State the blood parasite species.
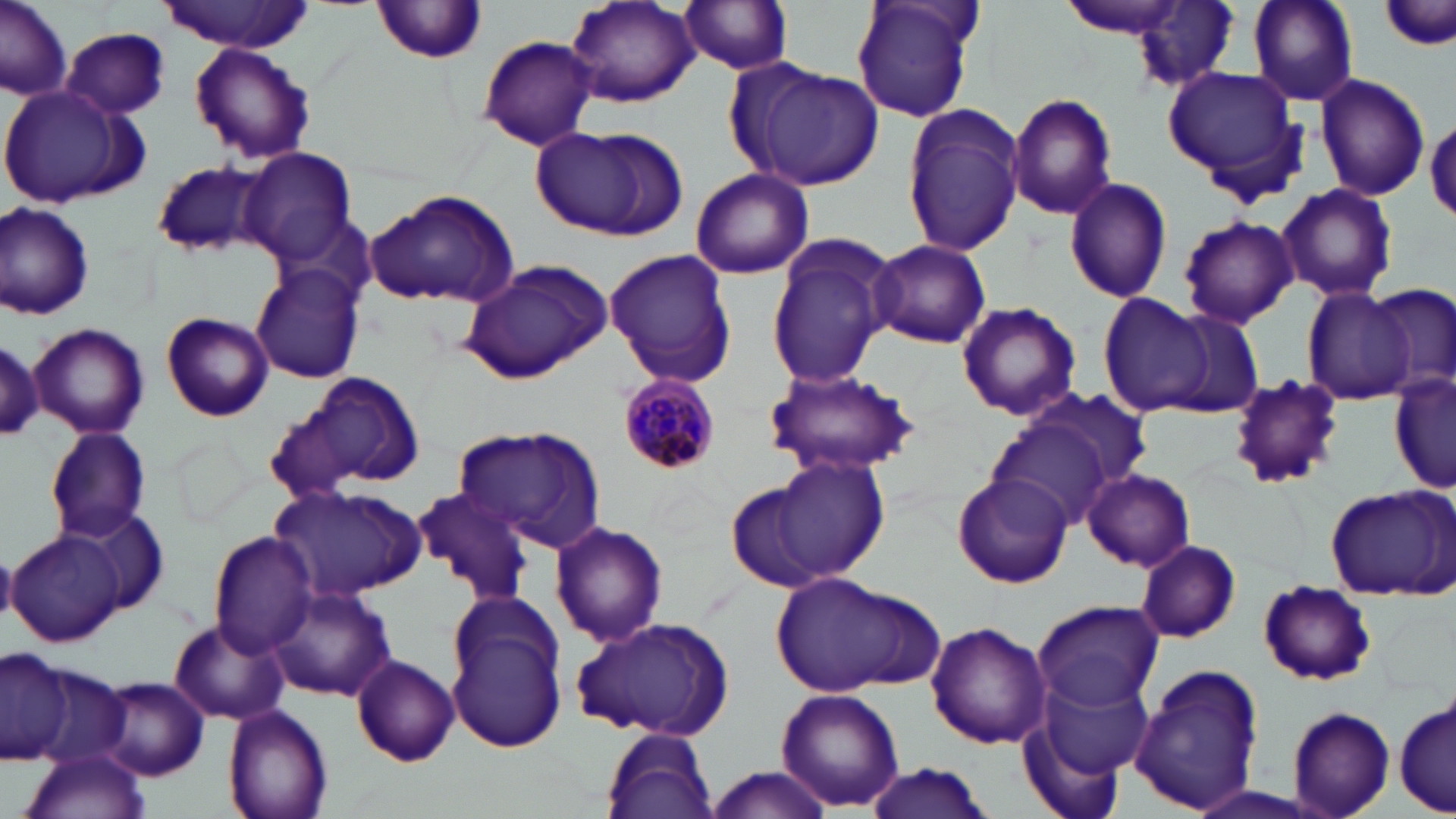

Plasmodium malariae.

Summary:
  - Coordinate format: approximate bounding boxes as (x1,y1)-(x2,y2) corner pairs in pixels
  - Plasmodium malariae-infected red blood cell locations: (619,381)-(718,472)
  - Uninfected red blood cell locations: (0,0)-(72,99), (562,0)-(700,107), (849,0)-(983,125), (1248,0)-(1358,106), (678,1)-(797,74), (1378,1)-(1456,53), (159,2)-(316,52), (371,2)-(489,65), (1127,2)-(1243,91), (60,26)-(172,119), (477,35)-(599,152), (190,44)-(316,164), (744,64)-(886,189), (1162,68)-(1304,177), (1314,71)-(1430,201), (0,85)-(150,208), (1007,91)-(1118,218), (901,104)-(1026,258), (1426,114)-(1456,221), (531,125)-(681,240), (237,146)-(358,264), (150,159)-(271,259), (690,169)-(814,279), (1063,175)-(1173,304), (1277,182)-(1399,302), (364,189)-(521,309), (0,200)-(96,320), (1177,215)-(1298,329), (762,236)-(896,389), (869,239)-(991,349), (604,247)-(736,388), (458,259)-(612,384), (251,265)-(366,384), (1369,282)-(1456,395), (1303,288)-(1415,402), (1098,293)-(1213,416), (956,300)-(1082,421), (1159,309)-(1267,419), (160,312)-(273,421), (28,323)-(149,439), (0,340)-(46,440), (765,366)-(920,479), (1388,370)-(1456,496), (307,371)-(426,488), (1226,374)-(1347,491), (1020,386)-(1157,498), (262,400)-(366,507), (987,419)-(1116,530), (451,425)-(606,551), (44,426)-(151,543), (771,458)-(889,580), (1081,468)-(1196,572), (952,471)-(1073,590), (724,478)-(834,596), (270,483)-(422,600), (413,484)-(536,603), (1324,484)-(1453,600), (68,506)-(172,619), (550,521)-(668,648), (7,529)-(124,645), (208,531)-(317,656), (1135,540)-(1241,643), (772,575)-(937,699), (1256,580)-(1378,687), (267,584)-(396,702), (1030,599)-(1162,712), (445,613)-(567,754), (570,615)-(737,742), (170,617)-(286,727), (925,622)-(1053,751), (0,650)-(75,763), (350,655)-(461,767), (20,661)-(136,771), (1127,664)-(1265,817), (1037,672)-(1157,785), (98,676)-(208,780), (775,687)-(905,811), (1393,694)-(1454,818), (223,705)-(334,819), (1286,706)-(1395,819), (1019,708)-(1137,819), (603,726)-(720,819), (17,750)-(153,819), (863,763)-(995,819), (700,766)-(839,818)
  - Image size: 1456×819 pixels
  - Stain: May-Grünwald-Giemsa
  - Modality: optical microscopy
  - Magnification: 1000x
  - Field of view: one of a larger specimen
  - Preparation: thin blood smear